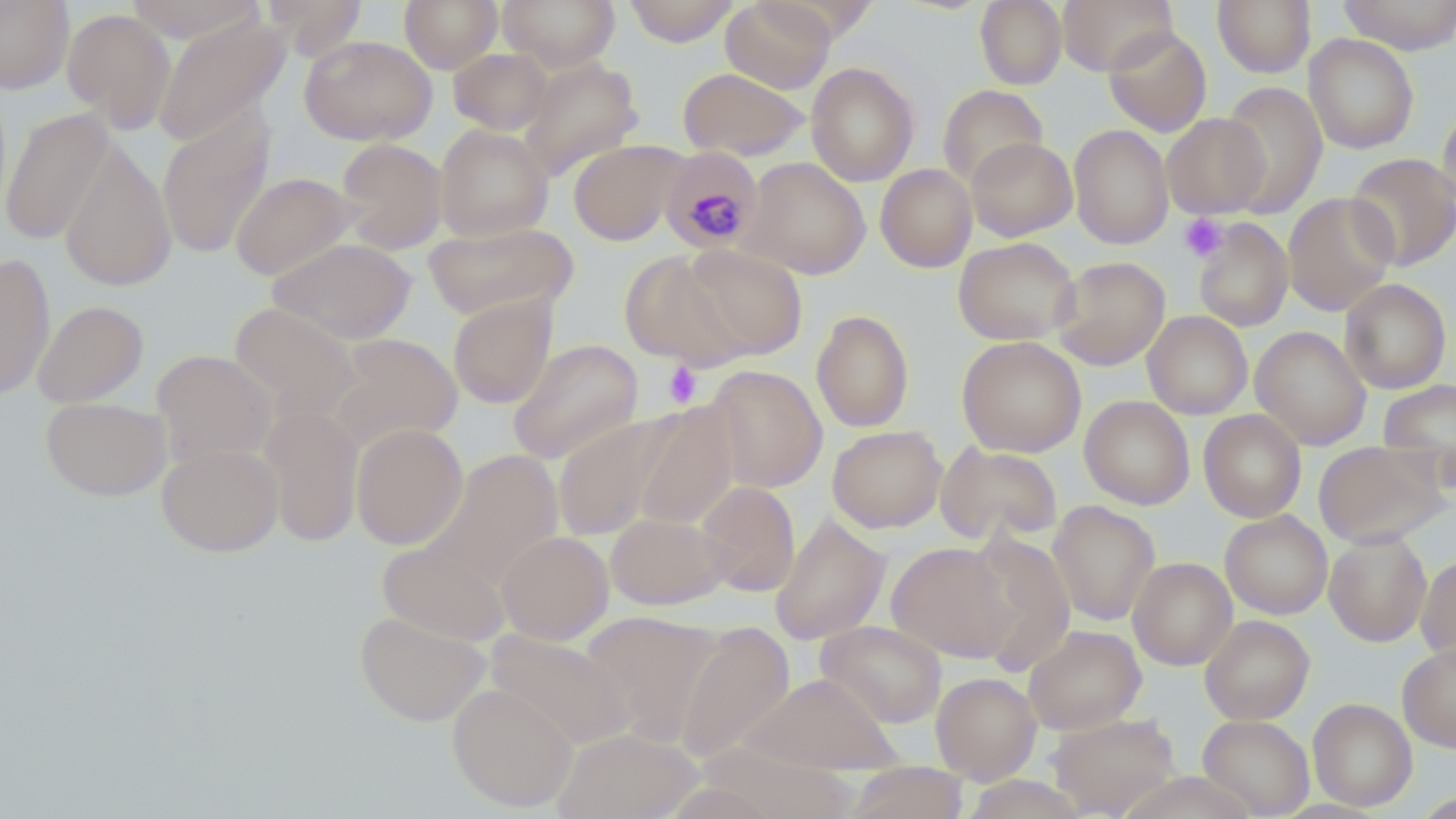

{
  "slide_level_diagnosis": "Plasmodium malariae",
  "preparation": "thin blood smear",
  "stain": "May-Grünwald-Giemsa",
  "magnification": "1000x",
  "plasmodium_malariae_infected_red_blood_cell_locations": "approximate bounding boxes as named x1/y1/x2/y2 corners in pixels: (x1=660, y1=147, x2=763, y2=254)",
  "field_of_view": "one of a larger specimen",
  "uninfected_red_blood_cell_locations": "approximate bounding boxes as named x1/y1/x2/y2 corners in pixels: (x1=0, y1=0, x2=74, y2=93), (x1=124, y1=0, x2=265, y2=43), (x1=261, y1=0, x2=368, y2=59), (x1=400, y1=0, x2=503, y2=73), (x1=498, y1=0, x2=620, y2=71), (x1=623, y1=0, x2=741, y2=46), (x1=720, y1=0, x2=836, y2=93), (x1=755, y1=0, x2=881, y2=44), (x1=975, y1=0, x2=1067, y2=89), (x1=1057, y1=0, x2=1177, y2=75), (x1=1212, y1=0, x2=1316, y2=77), (x1=1339, y1=0, x2=1456, y2=55), (x1=61, y1=8, x2=176, y2=133), (x1=153, y1=14, x2=290, y2=147), (x1=1102, y1=26, x2=1212, y2=137), (x1=1303, y1=33, x2=1419, y2=153), (x1=299, y1=34, x2=437, y2=146), (x1=448, y1=48, x2=552, y2=135), (x1=518, y1=57, x2=645, y2=180), (x1=806, y1=62, x2=919, y2=186), (x1=677, y1=67, x2=808, y2=161), (x1=1218, y1=82, x2=1327, y2=217), (x1=938, y1=84, x2=1048, y2=188), (x1=1437, y1=103, x2=1456, y2=218), (x1=1, y1=107, x2=116, y2=245), (x1=157, y1=109, x2=275, y2=259), (x1=1161, y1=113, x2=1270, y2=218), (x1=1068, y1=123, x2=1174, y2=249), (x1=434, y1=124, x2=554, y2=242), (x1=966, y1=136, x2=1077, y2=241), (x1=58, y1=137, x2=176, y2=292), (x1=334, y1=138, x2=448, y2=254), (x1=568, y1=139, x2=687, y2=246), (x1=1346, y1=153, x2=1456, y2=270), (x1=741, y1=157, x2=871, y2=278), (x1=875, y1=164, x2=977, y2=272), (x1=230, y1=172, x2=357, y2=281), (x1=1282, y1=191, x2=1398, y2=316), (x1=1193, y1=218, x2=1293, y2=332), (x1=422, y1=219, x2=578, y2=321), (x1=267, y1=237, x2=417, y2=344), (x1=953, y1=237, x2=1080, y2=345), (x1=681, y1=245, x2=807, y2=361), (x1=619, y1=250, x2=747, y2=367), (x1=0, y1=253, x2=55, y2=400), (x1=1051, y1=256, x2=1170, y2=370), (x1=1339, y1=278, x2=1452, y2=394), (x1=448, y1=295, x2=557, y2=408), (x1=32, y1=300, x2=148, y2=407), (x1=228, y1=302, x2=360, y2=422), (x1=811, y1=309, x2=914, y2=432), (x1=1143, y1=311, x2=1253, y2=419), (x1=1250, y1=325, x2=1371, y2=450), (x1=330, y1=333, x2=463, y2=451), (x1=957, y1=335, x2=1086, y2=457), (x1=507, y1=338, x2=644, y2=465), (x1=151, y1=349, x2=276, y2=466), (x1=705, y1=365, x2=827, y2=492), (x1=1379, y1=377, x2=1456, y2=485), (x1=1080, y1=395, x2=1194, y2=509), (x1=40, y1=397, x2=171, y2=501), (x1=629, y1=402, x2=738, y2=530), (x1=260, y1=406, x2=364, y2=547), (x1=1199, y1=409, x2=1306, y2=522), (x1=552, y1=414, x2=678, y2=541), (x1=351, y1=423, x2=468, y2=550), (x1=827, y1=425, x2=947, y2=532), (x1=1314, y1=440, x2=1448, y2=548), (x1=935, y1=441, x2=1063, y2=546), (x1=157, y1=444, x2=282, y2=556), (x1=427, y1=449, x2=564, y2=589), (x1=694, y1=481, x2=801, y2=597), (x1=1047, y1=500, x2=1160, y2=625), (x1=1220, y1=510, x2=1333, y2=619), (x1=605, y1=511, x2=729, y2=610), (x1=770, y1=512, x2=890, y2=645), (x1=497, y1=530, x2=613, y2=644), (x1=1324, y1=531, x2=1432, y2=646), (x1=962, y1=533, x2=1076, y2=673), (x1=378, y1=541, x2=510, y2=646), (x1=886, y1=542, x2=1015, y2=662), (x1=1416, y1=552, x2=1456, y2=664), (x1=1128, y1=557, x2=1237, y2=669), (x1=354, y1=609, x2=490, y2=726), (x1=580, y1=610, x2=724, y2=746), (x1=1199, y1=614, x2=1314, y2=724), (x1=816, y1=620, x2=947, y2=727), (x1=675, y1=622, x2=795, y2=764), (x1=1023, y1=625, x2=1146, y2=734), (x1=485, y1=628, x2=633, y2=750), (x1=1397, y1=642, x2=1456, y2=752), (x1=931, y1=672, x2=1041, y2=783), (x1=741, y1=673, x2=902, y2=774), (x1=447, y1=683, x2=578, y2=812), (x1=1308, y1=698, x2=1417, y2=810), (x1=1046, y1=712, x2=1181, y2=817), (x1=1198, y1=715, x2=1314, y2=817), (x1=553, y1=727, x2=702, y2=819), (x1=843, y1=761, x2=969, y2=818)",
  "image_size": "1456×819 pixels",
  "modality": "light microscopy",
  "platelet_locations": "approximate bounding boxes as named x1/y1/x2/y2 corners in pixels: (x1=1178, y1=213, x2=1228, y2=262), (x1=662, y1=361, x2=703, y2=408)"
}